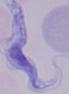

{
  "modality": "photomicrograph",
  "magnification": "1000x",
  "identification": "trypanosome"
}